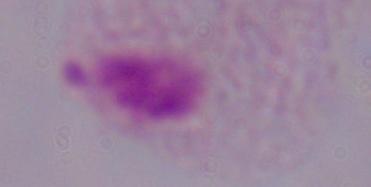 Captured at 1000x magnification. A trichomonad is seen. Photomicrograph.